Give the extent of all Babesia divergens-infected red blood cells.
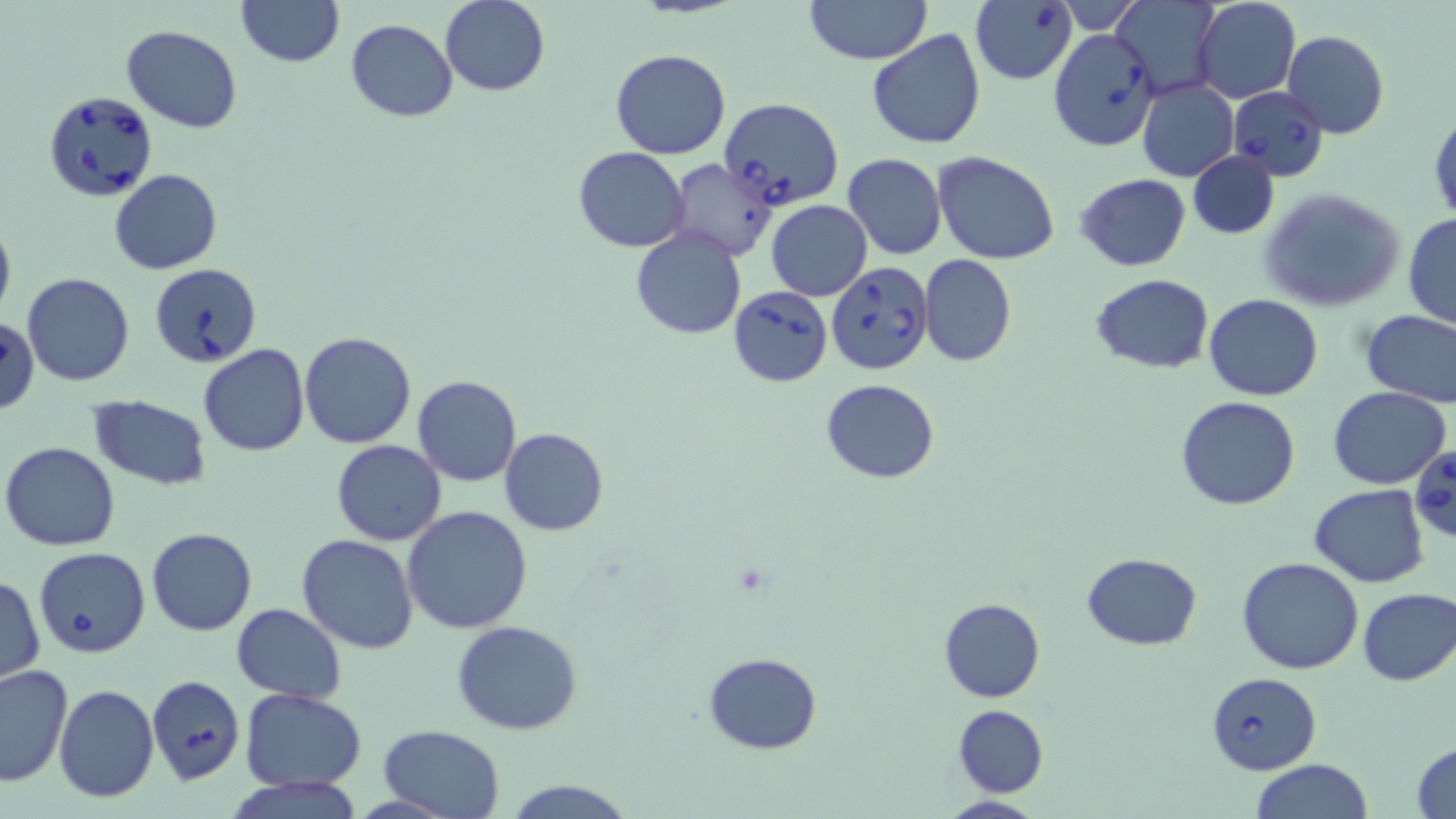

Approximate bounding boxes as [x1, y1, x2, y2] in pixels.
Babesia divergens-infected red blood cells: [969, 2, 1076, 87], [1049, 29, 1160, 151], [1226, 86, 1329, 181], [43, 90, 159, 204], [719, 98, 844, 209], [826, 262, 933, 377], [149, 263, 262, 368], [729, 286, 832, 387], [0, 318, 40, 414], [1408, 446, 1456, 545], [33, 547, 151, 658], [1207, 671, 1322, 773].

{
  "slide_level_diagnosis": "Babesia divergens",
  "preparation": "thin blood smear",
  "image_size": "1456×819 pixels",
  "uninfected_red_blood_cell_locations": "approximate bounding boxes as [x1, y1, x2, y2] in pixels: [236, 0, 343, 67], [1193, 0, 1301, 103], [441, 1, 549, 96], [803, 1, 932, 65], [1114, 1, 1220, 93], [346, 19, 457, 122], [121, 25, 244, 131], [866, 28, 987, 150], [1283, 30, 1389, 139], [610, 49, 731, 159], [1138, 80, 1238, 182], [1430, 108, 1455, 227], [574, 146, 688, 251], [1188, 151, 1278, 239], [934, 152, 1059, 264], [843, 153, 947, 259], [668, 158, 777, 262], [108, 168, 224, 275], [1075, 173, 1192, 272], [1260, 188, 1406, 313], [766, 200, 873, 301], [0, 214, 15, 323], [1402, 214, 1456, 330], [630, 229, 746, 339], [919, 254, 1017, 367], [21, 272, 135, 387], [1087, 273, 1213, 374], [1203, 293, 1324, 401], [1360, 308, 1456, 409], [300, 330, 416, 448], [199, 345, 309, 457], [412, 375, 523, 487], [822, 378, 940, 483], [1327, 386, 1451, 489], [88, 395, 212, 489], [1175, 396, 1301, 511], [499, 428, 608, 536], [331, 439, 447, 546], [2, 441, 122, 551], [1309, 485, 1429, 588], [403, 506, 533, 632], [146, 528, 258, 636], [297, 534, 419, 656], [1082, 552, 1202, 651], [1237, 557, 1366, 675], [1, 575, 45, 685], [1356, 587, 1455, 686], [939, 597, 1044, 702], [231, 603, 346, 706], [452, 620, 584, 734], [704, 652, 823, 753], [0, 665, 75, 787], [146, 676, 244, 786], [54, 684, 159, 802], [240, 689, 367, 791], [953, 705, 1048, 797], [378, 723, 507, 819], [1411, 741, 1456, 818], [1250, 760, 1375, 818], [504, 779, 636, 818], [938, 794, 1048, 818]",
  "field_of_view": "one of a larger specimen",
  "magnification": "1000x",
  "modality": "optical microscopy",
  "stain": "May-Grünwald-Giemsa"
}